Assess this cell for malaria.
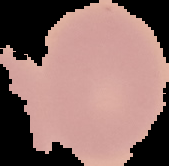

It is uninfected.

Image is 169×166 pixels. Segmented cell region on a black background. From a thin blood film.